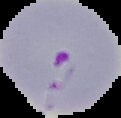
image size = 121×118 pixels
result = malaria parasites identified
image type = cell region segmented out of the field of view; surrounding area masked to black
preparation = thin blood smear